Assess for parasitized red blood cells.
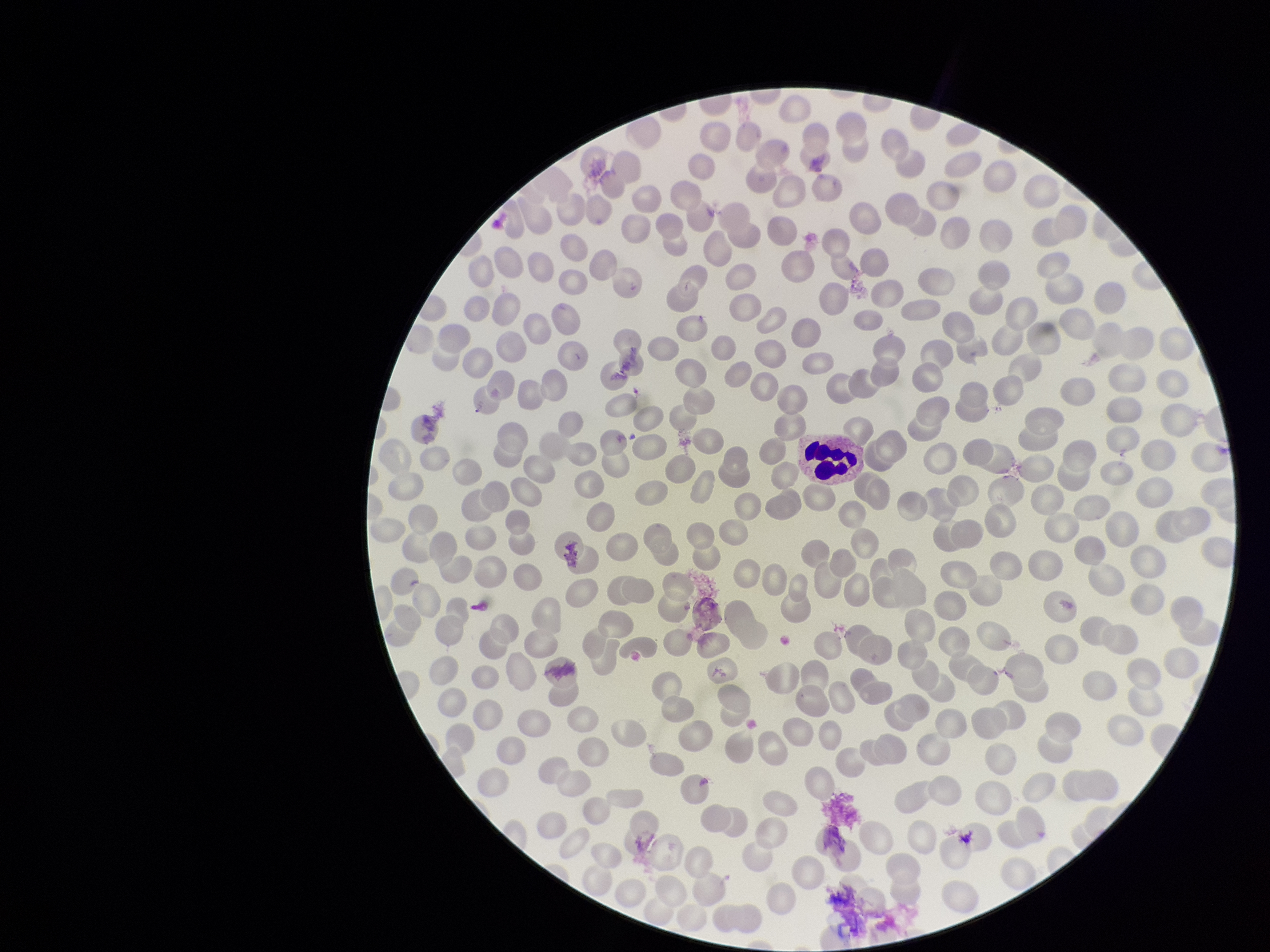

None identified.

Image is 1270×952 pixels. Parasitized red blood cell count: 0. Red blood cell count: 278. Giemsa stain. Preparation: thin smear. One field from this slide. Photographed through the microscope eyepiece with a smartphone camera. Patient malaria status: negative.